Describe the morphology of the red blood cells.
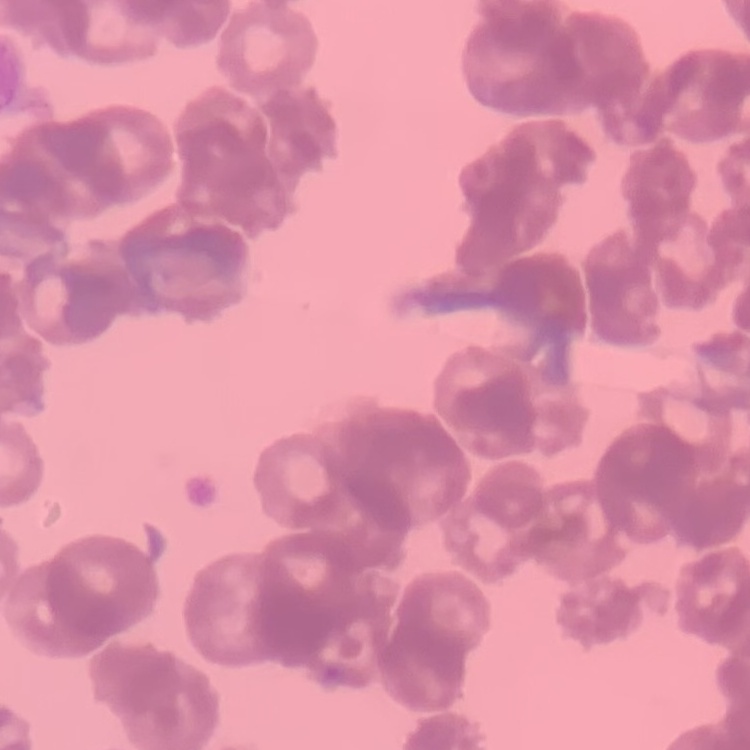

Rouleaux formation.

One tile cut from a larger photomicrograph. Thin peripheral smear. Stained with either Field's or Giemsa.